Identify the parasite.
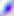

Toxoplasma gondii.

Summary:
  - Modality: photomicrograph
  - Magnification: 400x